Assess this cell for malaria.
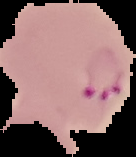

It is parasitized.

From a thin blood film. Segmented cell region on a black background. Image is 136×157 pixels.